Identify the parasite.
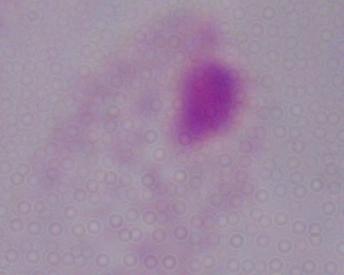

A trichomonad.

Captured at 1000x magnification. Photomicrograph.